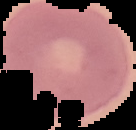

Summary:
  - Result: negative for malaria parasites
  - Image size: 136×130 pixels
  - Image type: segmented cell region on a black background
  - Preparation: thin blood film